Assess this cell for malaria.
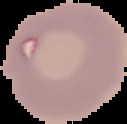
It is uninfected.

image_size: 127×124 pixels
image_type: cell region segmented out of the field of view; surrounding area masked to black
preparation: thin blood smear